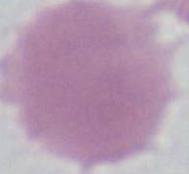
Summary:
  - Magnification: 1000x
  - Modality: micrograph
  - Identification: red blood cell